Give the position of every leukocyte visible.
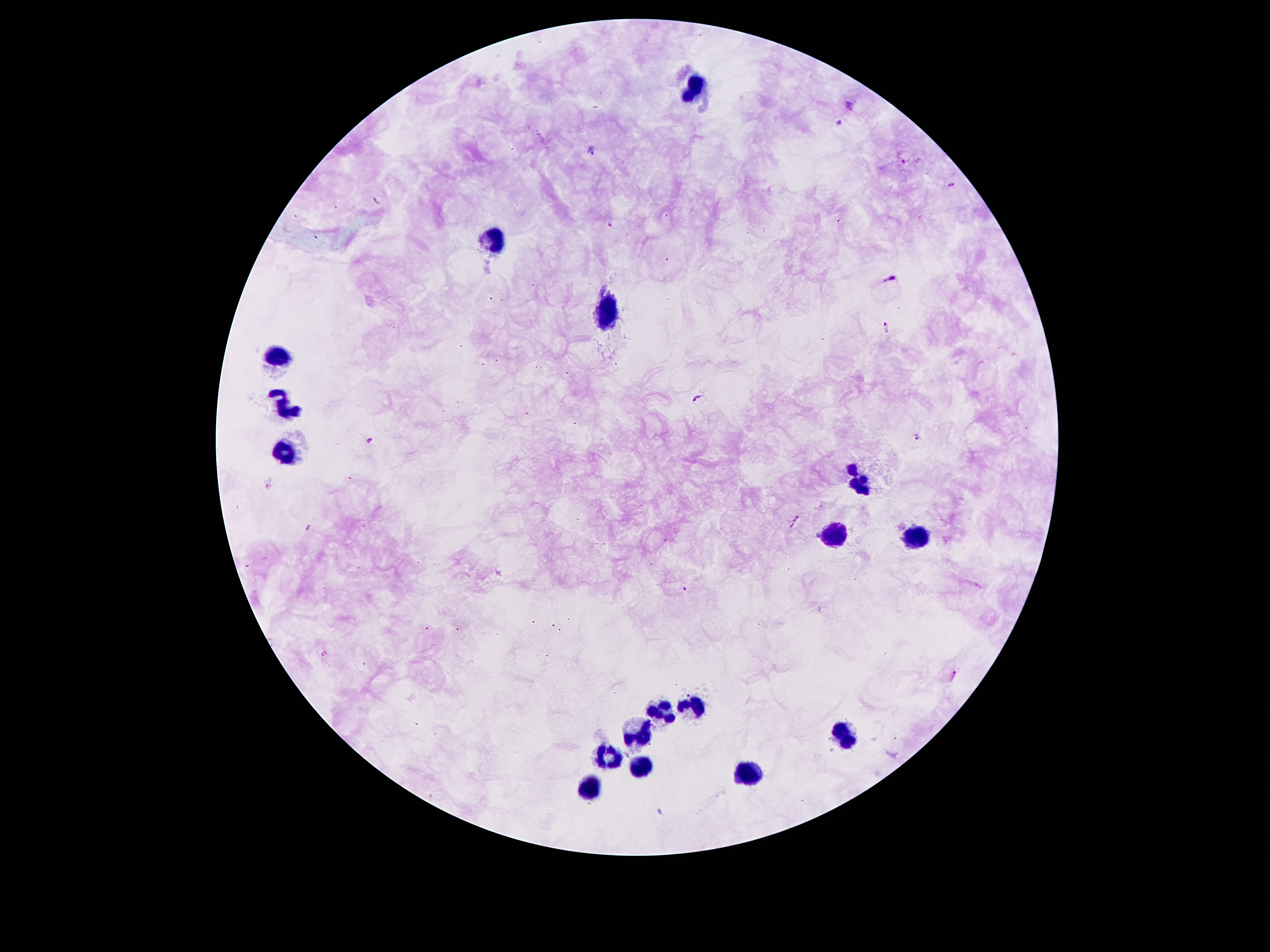

Approximate object centers, in pixels from the top-left corner.
Leukocytes: (x=696, y=86), (x=492, y=240), (x=608, y=311), (x=279, y=357), (x=288, y=406), (x=285, y=453), (x=862, y=481), (x=833, y=532), (x=917, y=538), (x=696, y=707), (x=664, y=712), (x=637, y=730), (x=842, y=735), (x=608, y=754), (x=639, y=768), (x=746, y=774), (x=590, y=790).

Plasmodium parasite locations: (x=848, y=105), (x=839, y=124), (x=592, y=151), (x=902, y=161), (x=951, y=185), (x=890, y=277), (x=888, y=326), (x=697, y=398), (x=920, y=437), (x=371, y=441), (x=795, y=522), (x=685, y=590), (x=955, y=676). Smartphone photograph taken through the microscope eyepiece. Patient malaria status: positive for Plasmodium falciparum. Image is 1270×952 pixels. Thick peripheral-blood smear. Giemsa stain. Single field of view. 100x magnification.